Point out each Plasmodium parasite.
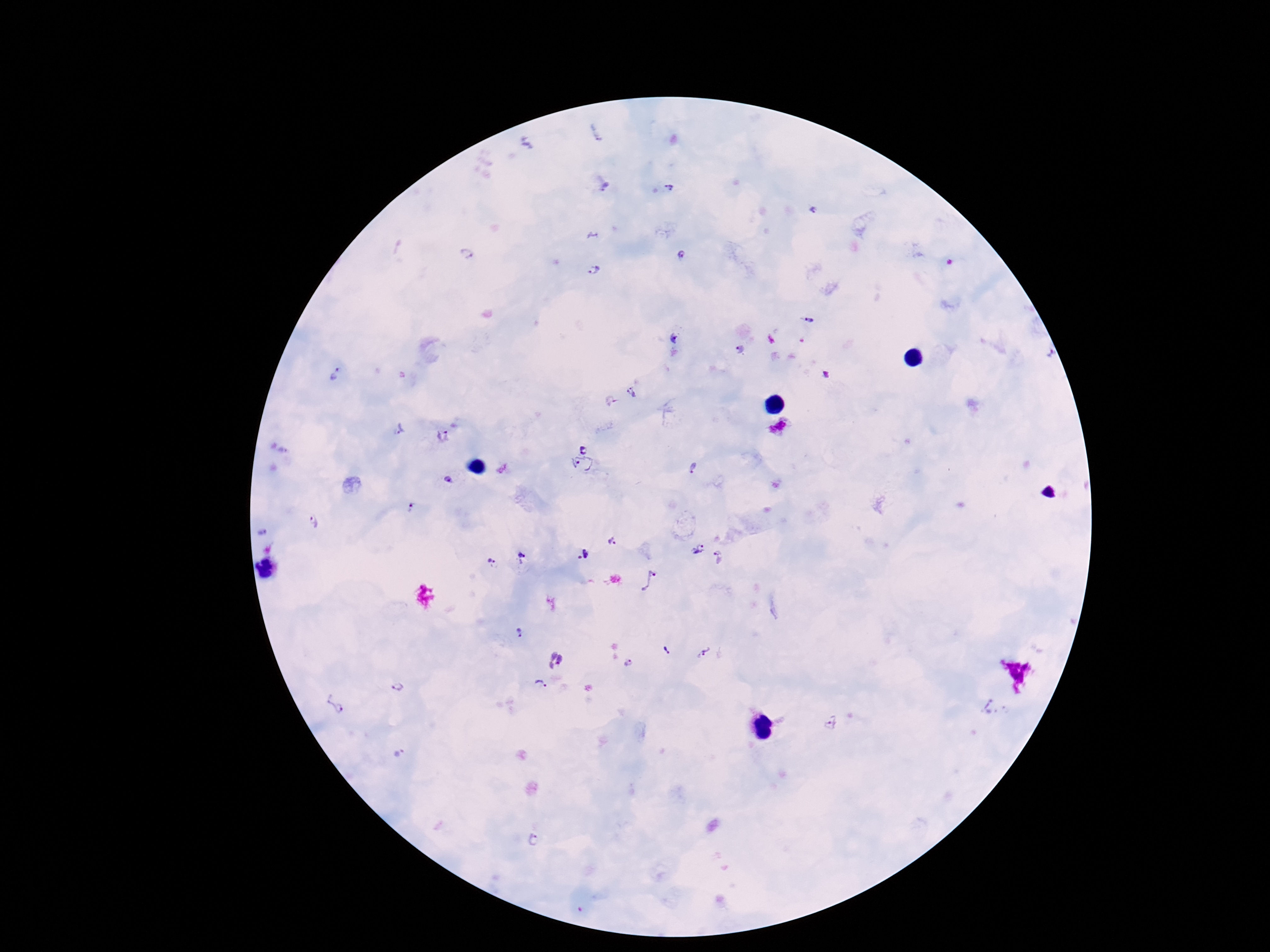
Approximate centers as (x, y) in pixels.
Plasmodium parasites: (604, 187), (669, 188), (813, 210), (680, 254), (466, 255), (594, 270), (809, 320), (675, 337), (741, 350), (1050, 354), (335, 374), (632, 394), (398, 429), (443, 437), (583, 446), (582, 465), (694, 469), (449, 481), (413, 507), (314, 522), (264, 532), (612, 542), (699, 550), (583, 556), (522, 557), (718, 557), (490, 562), (649, 582), (519, 634), (666, 651), (703, 652), (555, 659), (629, 664), (542, 684), (397, 687), (334, 705), (830, 722), (400, 752), (535, 839).

stain = Giemsa
field of view = single
preparation = thick peripheral-blood smear
image size = 1270×952 pixels
magnification = 100x
patient malaria status = infected
capture = smartphone camera through the microscope eyepiece